Locate and identify every blood parasite.
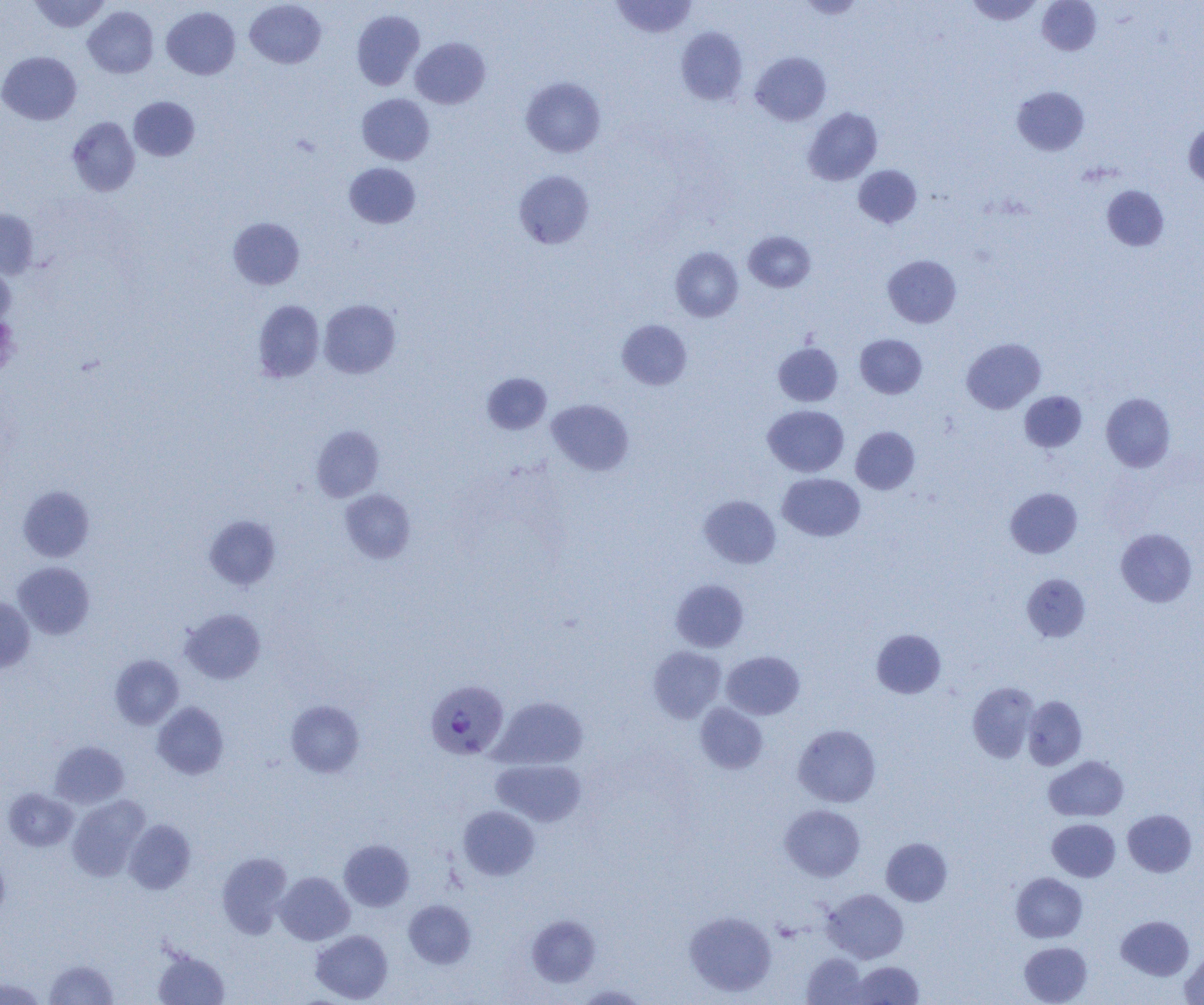
Approximate bounding boxes as named x1/y1/x2/y2 corners in pixels.
Plasmodium vivax-infected red blood cells: (x1=425, y1=680, x2=509, y2=760).
No Plasmodium falciparum, Plasmodium ovale, Plasmodium malariae, Babesia divergens, or Trypanosoma brucei observed.

Summary:
  - Uninfected red blood cell locations: (x1=29, y1=0, x2=110, y2=33), (x1=611, y1=0, x2=697, y2=39), (x1=798, y1=0, x2=866, y2=19), (x1=965, y1=0, x2=1044, y2=25), (x1=1037, y1=0, x2=1101, y2=55), (x1=245, y1=1, x2=326, y2=68), (x1=84, y1=6, x2=158, y2=78), (x1=162, y1=6, x2=240, y2=79), (x1=352, y1=10, x2=425, y2=90), (x1=676, y1=27, x2=748, y2=105), (x1=411, y1=37, x2=490, y2=109), (x1=0, y1=51, x2=82, y2=125), (x1=750, y1=52, x2=831, y2=125), (x1=521, y1=77, x2=605, y2=157), (x1=1012, y1=86, x2=1089, y2=156), (x1=357, y1=94, x2=434, y2=165), (x1=129, y1=96, x2=200, y2=161), (x1=803, y1=107, x2=882, y2=185), (x1=67, y1=117, x2=140, y2=196), (x1=1184, y1=122, x2=1204, y2=188), (x1=344, y1=163, x2=420, y2=228), (x1=854, y1=165, x2=921, y2=228), (x1=514, y1=170, x2=594, y2=249), (x1=1102, y1=186, x2=1169, y2=251), (x1=0, y1=208, x2=38, y2=279), (x1=228, y1=217, x2=305, y2=290), (x1=744, y1=231, x2=816, y2=292), (x1=670, y1=247, x2=743, y2=322), (x1=883, y1=255, x2=961, y2=328), (x1=0, y1=261, x2=16, y2=327), (x1=319, y1=299, x2=400, y2=378), (x1=253, y1=300, x2=324, y2=382), (x1=617, y1=319, x2=692, y2=388), (x1=855, y1=334, x2=927, y2=398), (x1=961, y1=338, x2=1046, y2=413), (x1=773, y1=343, x2=843, y2=406), (x1=482, y1=373, x2=551, y2=434), (x1=1019, y1=391, x2=1087, y2=452), (x1=1101, y1=392, x2=1176, y2=472), (x1=547, y1=399, x2=634, y2=476), (x1=763, y1=405, x2=849, y2=476), (x1=311, y1=426, x2=384, y2=501), (x1=851, y1=426, x2=920, y2=494), (x1=778, y1=473, x2=865, y2=541), (x1=18, y1=486, x2=94, y2=562), (x1=1005, y1=487, x2=1082, y2=558), (x1=340, y1=489, x2=415, y2=562), (x1=699, y1=495, x2=781, y2=567), (x1=205, y1=515, x2=281, y2=590), (x1=1116, y1=528, x2=1197, y2=607), (x1=13, y1=562, x2=94, y2=639), (x1=1022, y1=573, x2=1091, y2=642), (x1=671, y1=580, x2=749, y2=652), (x1=0, y1=598, x2=35, y2=673), (x1=180, y1=608, x2=266, y2=684), (x1=872, y1=629, x2=946, y2=698), (x1=648, y1=646, x2=726, y2=723), (x1=721, y1=651, x2=805, y2=719), (x1=110, y1=654, x2=183, y2=729), (x1=967, y1=681, x2=1039, y2=763), (x1=491, y1=696, x2=588, y2=770), (x1=1023, y1=696, x2=1087, y2=770), (x1=286, y1=700, x2=365, y2=777), (x1=152, y1=701, x2=229, y2=779), (x1=695, y1=703, x2=768, y2=774), (x1=793, y1=725, x2=881, y2=807), (x1=50, y1=741, x2=130, y2=808), (x1=1044, y1=756, x2=1128, y2=821), (x1=491, y1=759, x2=586, y2=827), (x1=3, y1=788, x2=78, y2=851), (x1=67, y1=795, x2=150, y2=881), (x1=780, y1=804, x2=865, y2=881), (x1=458, y1=805, x2=540, y2=880), (x1=1123, y1=809, x2=1196, y2=877), (x1=1047, y1=818, x2=1120, y2=882), (x1=124, y1=819, x2=196, y2=894), (x1=881, y1=838, x2=952, y2=906), (x1=339, y1=839, x2=414, y2=911), (x1=216, y1=852, x2=293, y2=937), (x1=0, y1=854, x2=10, y2=923), (x1=275, y1=871, x2=354, y2=945), (x1=1011, y1=872, x2=1087, y2=942), (x1=823, y1=889, x2=908, y2=963), (x1=404, y1=900, x2=476, y2=968), (x1=685, y1=911, x2=777, y2=996), (x1=527, y1=915, x2=601, y2=986), (x1=1116, y1=915, x2=1194, y2=980), (x1=310, y1=929, x2=393, y2=1002), (x1=1019, y1=941, x2=1092, y2=1005), (x1=153, y1=949, x2=230, y2=1005), (x1=1180, y1=951, x2=1204, y2=1004), (x1=802, y1=953, x2=867, y2=1004), (x1=44, y1=959, x2=118, y2=1004), (x1=849, y1=961, x2=924, y2=1004), (x1=0, y1=976, x2=48, y2=1005), (x1=574, y1=983, x2=648, y2=1004)
  - Slide-level diagnosis: Plasmodium vivax
  - Magnification: 1000x
  - Image size: 1204×1005 pixels
  - Field of view: single
  - Modality: optical microscopy
  - Preparation: thin blood film